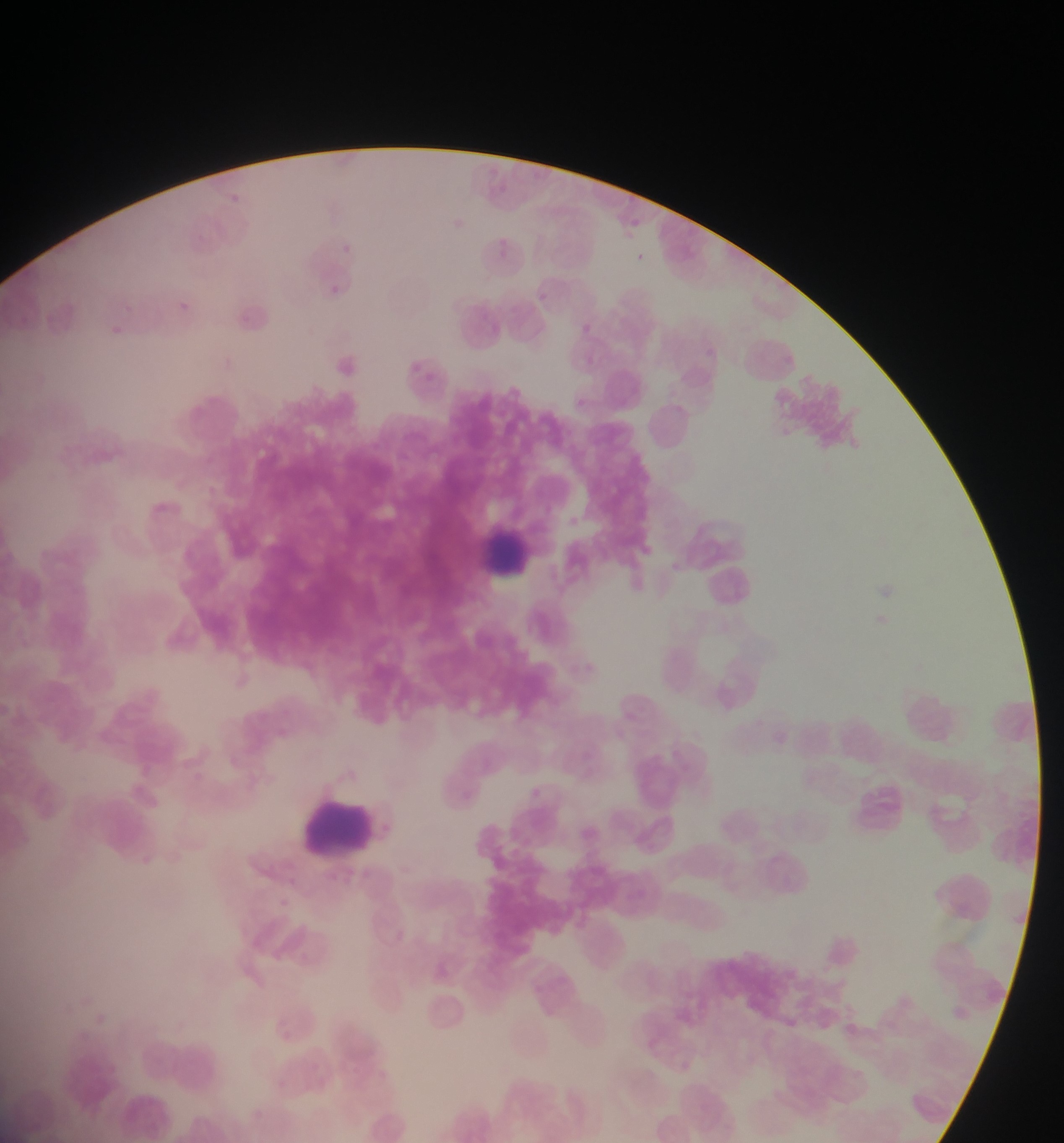

Approximate bounding boxes as [left, top, right, bottom] in pixels.
Summary:
  - Leukocyte locations: [473, 522, 547, 602], [297, 793, 390, 865]
  - Preparation: thin blood smear
  - Field of view: single
  - Image size: 1064×1143 pixels
  - Country: Ghana
  - Capture: mobile-phone photograph through a microscope